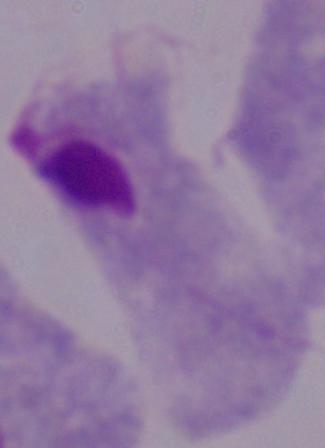
1000x magnification. A trichomonad is shown. Micrograph.